Locate every malaria parasite and every leukocyte.
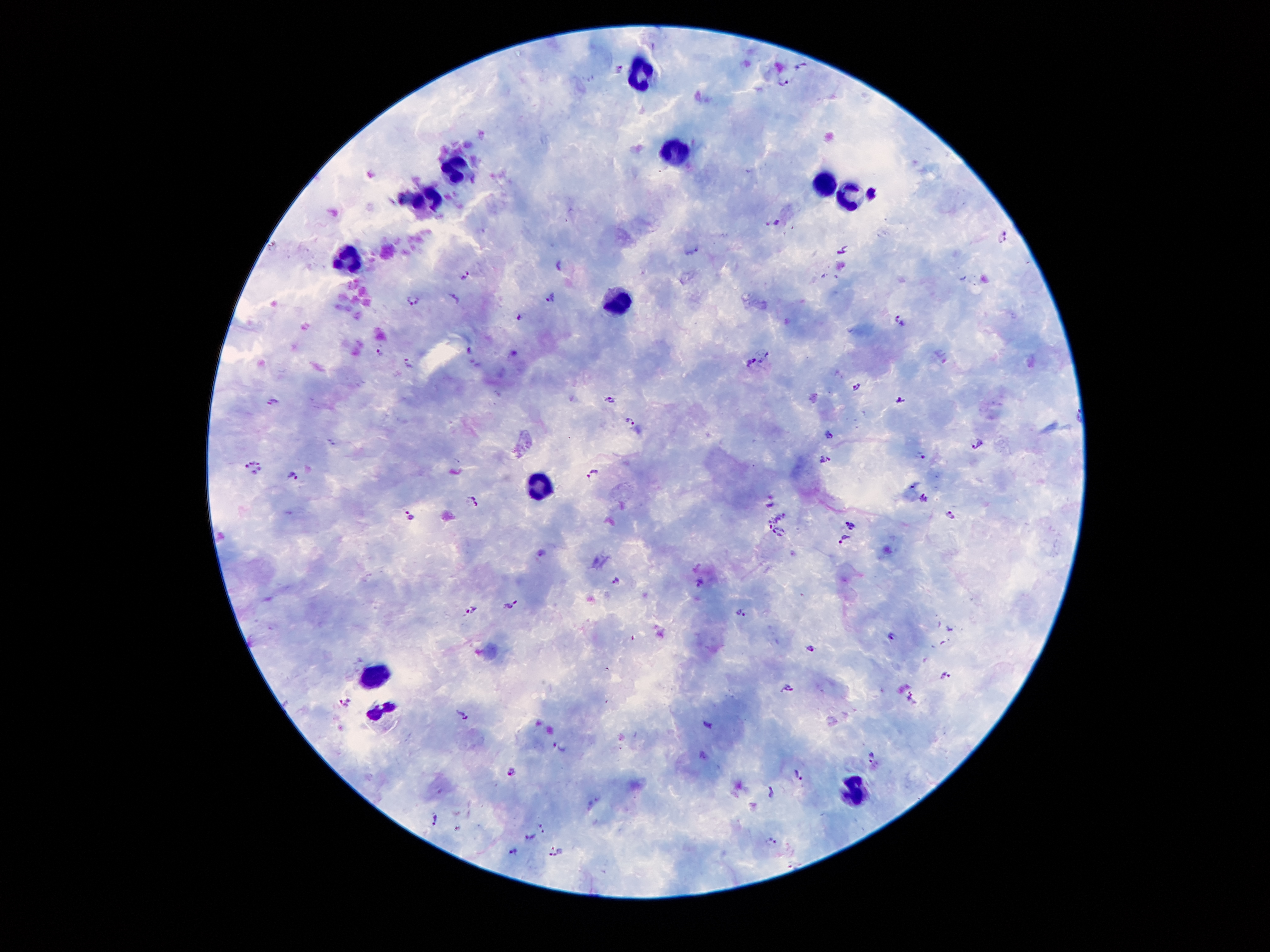
Approximate centers as [x, y] in pixels.
Malaria parasites: [785, 81], [775, 221], [1003, 237], [844, 250], [559, 265], [465, 274], [551, 299], [413, 300], [519, 317], [898, 319], [380, 351], [469, 353], [751, 363], [408, 364], [858, 387], [610, 400], [273, 401], [900, 402], [630, 424], [828, 434], [332, 442], [976, 446], [923, 458], [825, 459], [253, 467], [290, 475], [595, 476], [925, 500], [475, 503], [772, 504], [410, 517], [951, 517], [771, 522], [848, 526], [780, 534], [845, 543], [616, 581], [698, 581], [511, 605], [471, 608], [740, 614], [893, 635], [810, 647], [945, 677], [788, 688], [911, 696], [345, 704], [463, 714], [707, 725], [559, 748], [873, 755], [511, 773], [801, 775], [771, 792], [436, 819], [541, 826], [457, 832], [526, 836], [770, 842], [513, 850], [553, 855].
Leukocytes: [645, 74], [675, 158], [456, 171], [827, 182], [430, 197], [853, 197], [346, 262], [616, 300], [536, 488], [375, 675], [383, 711], [853, 794].

{
  "patient_malaria_status": "positive for Plasmodium falciparum",
  "field_of_view": "one from this slide",
  "preparation": "thick blood smear",
  "image_size": "1270×952 pixels",
  "stain": "Giemsa",
  "capture": "smartphone through the microscope eyepiece",
  "magnification": "100x"
}